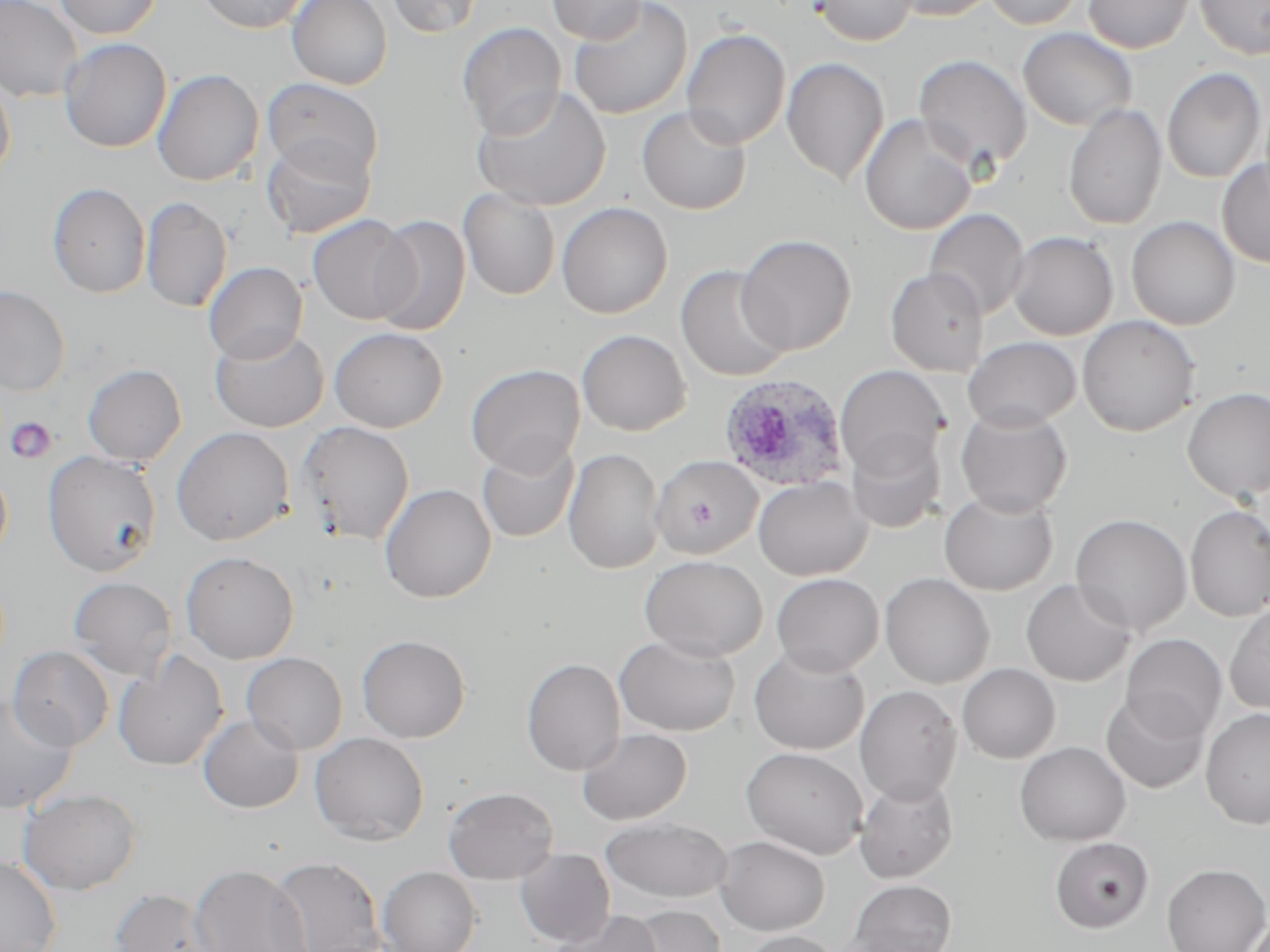

Approximate bounding boxes as (x1,y1)-(x2,y2) corner pairs in pixels. Plasmodium ovale-infected red blood cell locations: (718,374)-(851,492). Uninfected red blood cell locations: (0,0)-(83,102), (53,0)-(162,39), (195,0)-(310,34), (287,0)-(392,90), (386,0)-(483,38), (546,0)-(649,44), (567,0)-(693,120), (811,0)-(919,46), (889,0)-(999,21), (983,0)-(1086,30), (1083,0)-(1193,54), (1194,0)-(1270,60), (457,22)-(566,139), (1018,28)-(1137,130), (682,29)-(790,149), (59,37)-(171,153), (913,54)-(1033,174), (781,58)-(889,185), (152,68)-(264,186), (1162,68)-(1267,183), (0,72)-(15,187), (261,77)-(384,182), (471,84)-(612,212), (1063,103)-(1167,230), (636,106)-(752,215), (859,114)-(977,236), (261,134)-(376,239), (1217,158)-(1270,267), (47,182)-(151,298), (458,188)-(561,300), (141,196)-(232,313), (556,202)-(673,318), (924,209)-(1030,320), (307,213)-(417,325), (370,215)-(471,336), (1127,216)-(1240,330), (1007,231)-(1118,340), (735,234)-(856,355), (203,261)-(307,364), (675,265)-(793,382), (885,267)-(990,376), (0,285)-(70,396), (1078,315)-(1201,437), (210,327)-(329,432), (329,327)-(448,432), (577,329)-(691,436), (963,336)-(1082,431), (82,363)-(187,466), (466,363)-(585,475), (834,365)-(948,478), (1182,387)-(1270,502), (954,406)-(1073,516), (296,421)-(415,544), (171,426)-(294,546), (844,433)-(946,534), (477,438)-(579,543), (564,447)-(665,574), (42,451)-(162,577), (651,454)-(763,559), (0,466)-(12,562), (753,477)-(872,580), (380,483)-(497,603), (939,490)-(1059,595), (1185,505)-(1270,622), (1070,514)-(1192,635), (181,551)-(299,664), (639,554)-(768,661), (771,573)-(884,676), (879,573)-(995,689), (68,577)-(177,680), (1020,578)-(1137,687), (1224,601)-(1270,715), (356,634)-(471,743), (615,634)-(740,736), (1121,634)-(1227,741), (8,645)-(115,751), (749,646)-(869,754), (113,650)-(229,771), (242,652)-(348,754), (521,657)-(626,775), (957,663)-(1061,763), (854,684)-(962,804), (1101,691)-(1210,794), (0,694)-(79,814), (1200,708)-(1270,829), (198,715)-(304,813), (576,727)-(692,825), (310,732)-(429,845), (1014,742)-(1130,846), (741,746)-(869,859), (854,775)-(959,883), (443,786)-(558,885), (17,788)-(143,895), (599,817)-(733,904), (715,835)-(830,935), (1049,836)-(1154,933), (515,848)-(616,948), (267,855)-(386,952), (0,856)-(62,952), (189,863)-(311,952), (1162,863)-(1270,952), (378,866)-(482,952), (847,879)-(957,952), (109,887)-(220,952), (624,904)-(726,952), (547,909)-(663,952), (739,930)-(845,952). Platelet locations: (6,417)-(58,464). Slide-level diagnosis: Plasmodium ovale. Single field of view. Thin blood smear. Image is 1270×952 pixels. May-Grünwald-Giemsa-stained preparation. Captured at 1000x magnification. Optical microscopy.